Give the extent of all Plasmodium ovale-infected red blood cells.
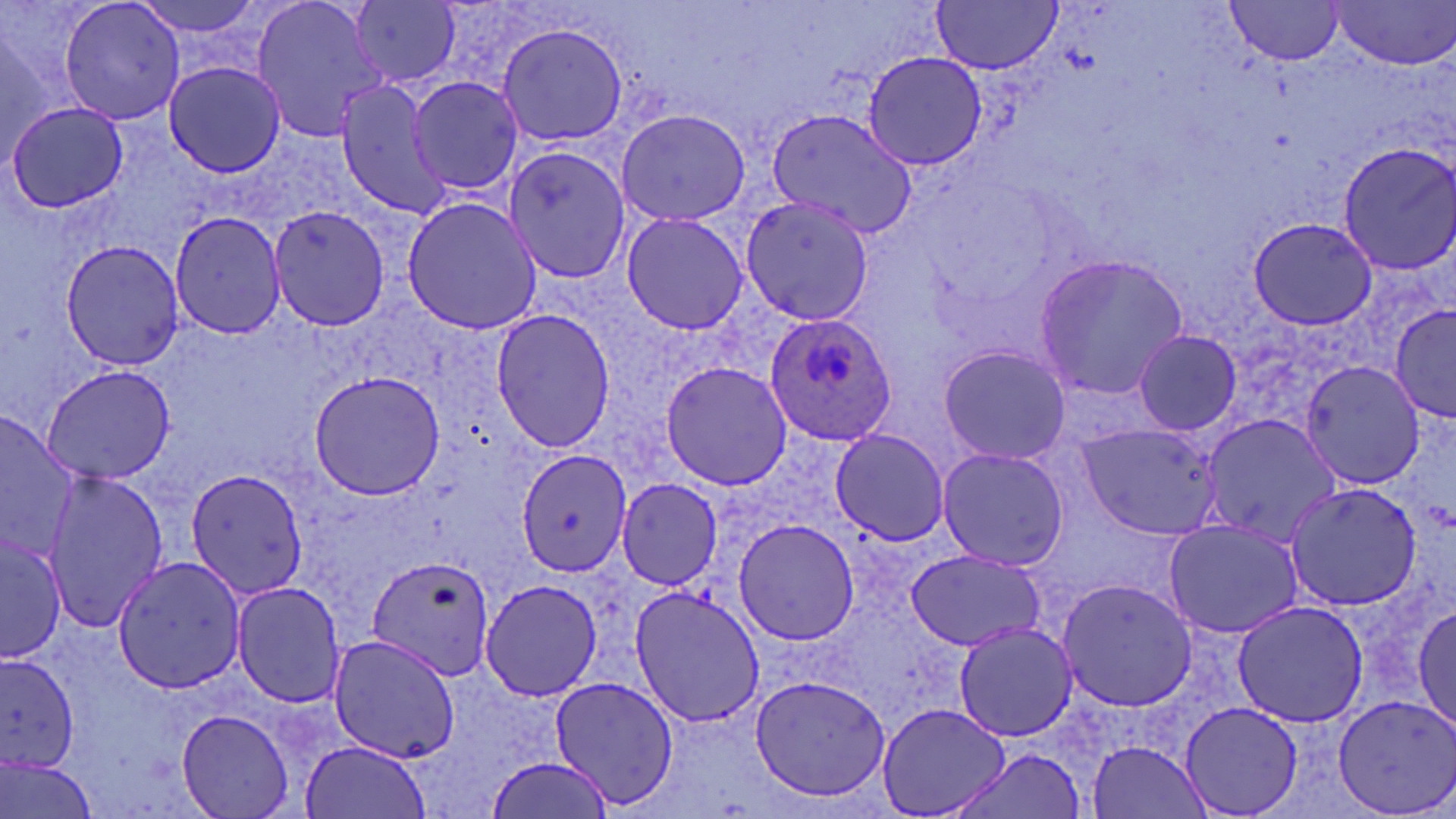

Approximate bounding boxes as [x1, y1, x2, y2] in pixels.
Plasmodium ovale-infected red blood cells: [765, 313, 899, 446].

Uninfected red blood cell locations: [58, 0, 186, 127], [131, 0, 274, 51], [249, 0, 389, 144], [931, 0, 1063, 73], [350, 1, 462, 87], [1226, 2, 1343, 67], [1333, 2, 1455, 70], [0, 13, 65, 168], [496, 21, 628, 149], [861, 50, 986, 171], [162, 60, 287, 178], [406, 75, 522, 196], [333, 81, 449, 218], [7, 101, 129, 213], [616, 107, 750, 228], [766, 107, 920, 237], [1335, 142, 1456, 275], [502, 146, 628, 287], [737, 195, 876, 324], [402, 197, 543, 337], [269, 204, 391, 331], [620, 211, 749, 336], [169, 213, 289, 339], [1248, 216, 1378, 331], [59, 238, 189, 371], [1032, 252, 1190, 400], [1393, 304, 1456, 419], [490, 308, 616, 452], [1132, 329, 1243, 436], [936, 343, 1072, 465], [1297, 358, 1426, 490], [661, 360, 792, 491], [39, 362, 178, 484], [309, 370, 444, 500], [0, 407, 78, 568], [1200, 412, 1341, 549], [1076, 423, 1221, 537], [830, 428, 951, 545], [936, 446, 1069, 570], [514, 448, 631, 578], [187, 469, 308, 600], [42, 470, 168, 629], [616, 479, 723, 591], [1284, 482, 1423, 611], [1164, 518, 1305, 639], [734, 519, 859, 644], [0, 530, 65, 661], [903, 549, 1046, 652], [113, 553, 246, 695], [366, 555, 495, 682], [1054, 576, 1199, 712], [479, 577, 603, 703], [231, 580, 346, 707], [627, 585, 767, 727], [1230, 600, 1368, 726], [1413, 602, 1455, 736], [953, 621, 1077, 742], [326, 634, 460, 762], [0, 652, 84, 778], [749, 672, 891, 804], [547, 675, 679, 813], [1333, 694, 1456, 817], [879, 702, 1010, 818], [1180, 702, 1303, 819], [177, 709, 295, 819], [301, 739, 433, 819], [1086, 739, 1214, 819], [944, 748, 1088, 819], [486, 750, 619, 819], [1, 753, 101, 819]. Slide-level diagnosis: Plasmodium ovale. Light microscopy. Captured at 1000x magnification. Thin blood smear. May-Grünwald-Giemsa stain. One field of a larger specimen. Image is 1456×819 pixels.